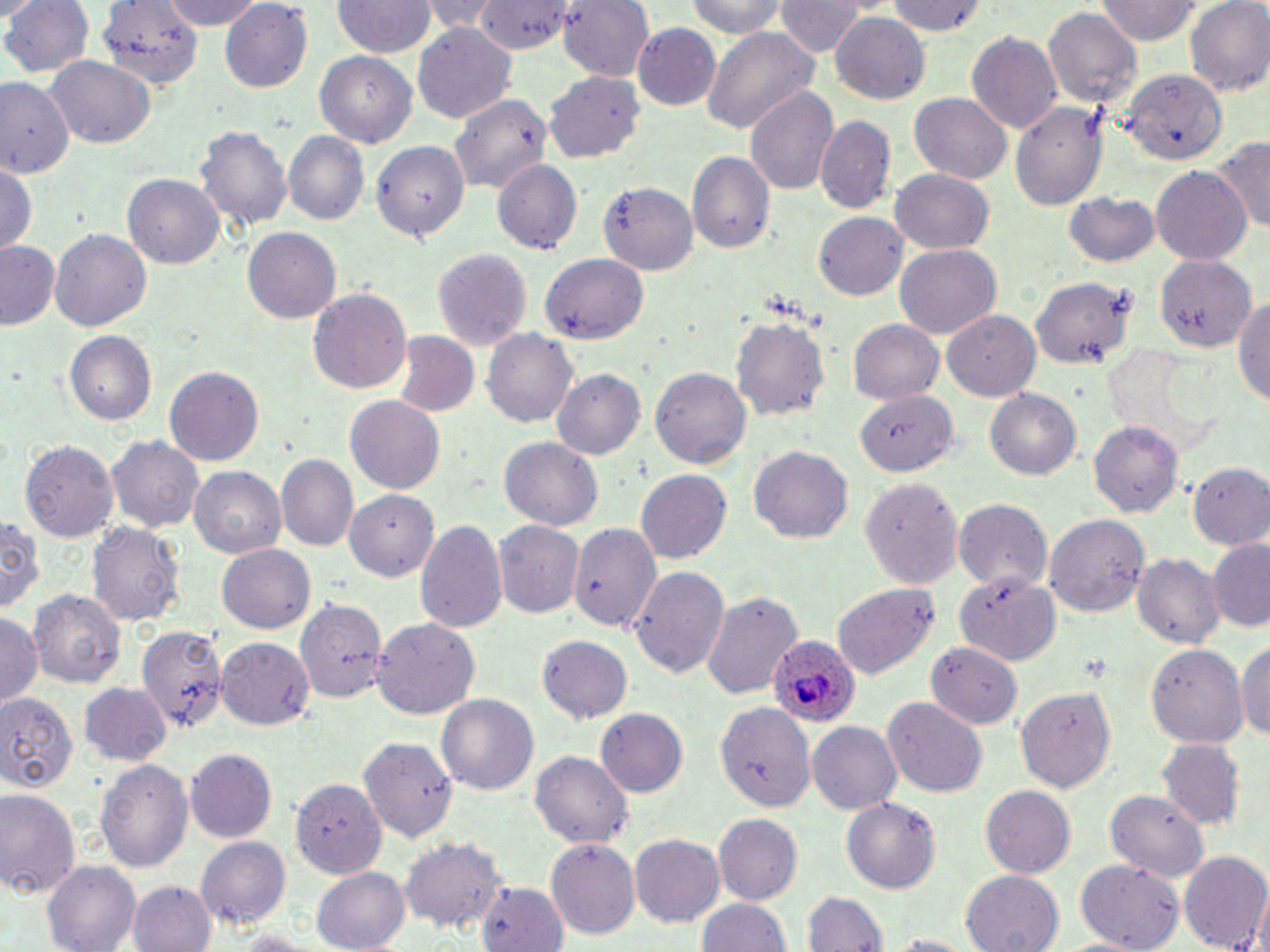
Approximate bounding boxes as (x1, y1, x2, y2) in pixels. Uninfected red blood cell locations: (1, 0, 93, 79), (162, 0, 265, 30), (424, 0, 505, 36), (559, 0, 656, 83), (681, 0, 792, 39), (774, 0, 864, 59), (1096, 0, 1200, 45), (1185, 0, 1270, 97), (332, 1, 434, 59), (884, 1, 990, 37), (101, 2, 199, 86), (219, 2, 312, 93), (471, 2, 579, 53), (1043, 8, 1141, 109), (830, 12, 929, 103), (413, 21, 518, 124), (633, 23, 720, 110), (699, 25, 822, 135), (964, 30, 1063, 135), (316, 52, 417, 149), (45, 54, 158, 148), (1121, 68, 1226, 165), (545, 71, 646, 162), (0, 76, 75, 179), (744, 86, 839, 196), (909, 95, 1010, 186), (450, 96, 551, 197), (1011, 99, 1105, 210), (815, 116, 895, 214), (197, 124, 292, 239), (282, 133, 368, 226), (367, 135, 471, 246), (1213, 135, 1270, 237), (688, 151, 775, 254), (491, 158, 584, 254), (0, 162, 38, 252), (1150, 166, 1252, 267), (892, 168, 994, 253), (123, 174, 225, 270), (601, 180, 700, 275), (1064, 193, 1161, 269), (814, 212, 907, 300), (244, 227, 340, 323), (50, 228, 151, 334), (1, 241, 59, 330), (894, 244, 1000, 341), (432, 248, 531, 351), (540, 253, 648, 342), (1154, 253, 1258, 352), (1031, 278, 1134, 369), (308, 289, 410, 396), (1235, 290, 1270, 409), (943, 310, 1042, 400), (731, 315, 829, 423), (849, 320, 943, 407), (483, 328, 578, 429), (66, 331, 156, 424), (391, 331, 479, 419), (165, 366, 263, 465), (651, 366, 750, 469), (551, 368, 646, 460), (986, 387, 1083, 482), (854, 393, 962, 476), (346, 396, 445, 495), (1089, 422, 1181, 518), (107, 434, 206, 534), (19, 436, 119, 541), (500, 437, 603, 532), (748, 445, 854, 543), (276, 455, 359, 551), (1187, 463, 1270, 549), (190, 465, 286, 559), (636, 470, 731, 565), (860, 479, 960, 590), (344, 490, 439, 581), (954, 498, 1052, 593), (0, 514, 42, 614), (1044, 514, 1149, 619), (415, 519, 507, 636), (495, 521, 584, 619), (89, 523, 186, 627), (573, 525, 671, 638), (1206, 538, 1270, 631), (216, 544, 315, 631), (1133, 553, 1222, 652), (629, 563, 728, 682), (955, 576, 1059, 665), (831, 582, 939, 683), (27, 588, 127, 691), (701, 589, 802, 703), (295, 594, 390, 701), (1, 615, 41, 706), (373, 619, 479, 719), (137, 625, 229, 731), (1238, 636, 1270, 746), (217, 637, 312, 729), (537, 637, 631, 723), (1147, 642, 1247, 745), (929, 643, 1023, 729), (78, 681, 172, 767), (1014, 686, 1117, 795), (0, 689, 81, 794), (436, 694, 537, 798), (882, 699, 986, 795), (719, 703, 816, 812), (596, 708, 687, 798), (807, 720, 904, 814), (359, 737, 455, 839), (1156, 738, 1245, 830), (187, 750, 275, 842), (530, 751, 633, 848), (95, 758, 192, 870), (291, 778, 384, 876), (980, 786, 1074, 878), (0, 789, 82, 901), (1104, 789, 1205, 881), (840, 796, 941, 893), (711, 813, 800, 905), (629, 833, 725, 927), (197, 836, 289, 931), (400, 836, 507, 936), (546, 836, 639, 938), (1179, 851, 1270, 952), (1075, 859, 1187, 950), (44, 861, 141, 951), (312, 865, 410, 952), (961, 868, 1064, 952), (129, 881, 215, 952), (473, 883, 566, 951), (803, 890, 886, 951), (695, 896, 791, 952). Plasmodium ovale-infected red blood cell locations: (767, 634, 860, 728). Slide-level diagnosis: Plasmodium ovale. Optical microscopy. Image is 1270×952 pixels. May-Grünwald-Giemsa stain. One field of a larger specimen. Thin blood film. 1000x magnification.